Locate every blood parasite and identify its species.
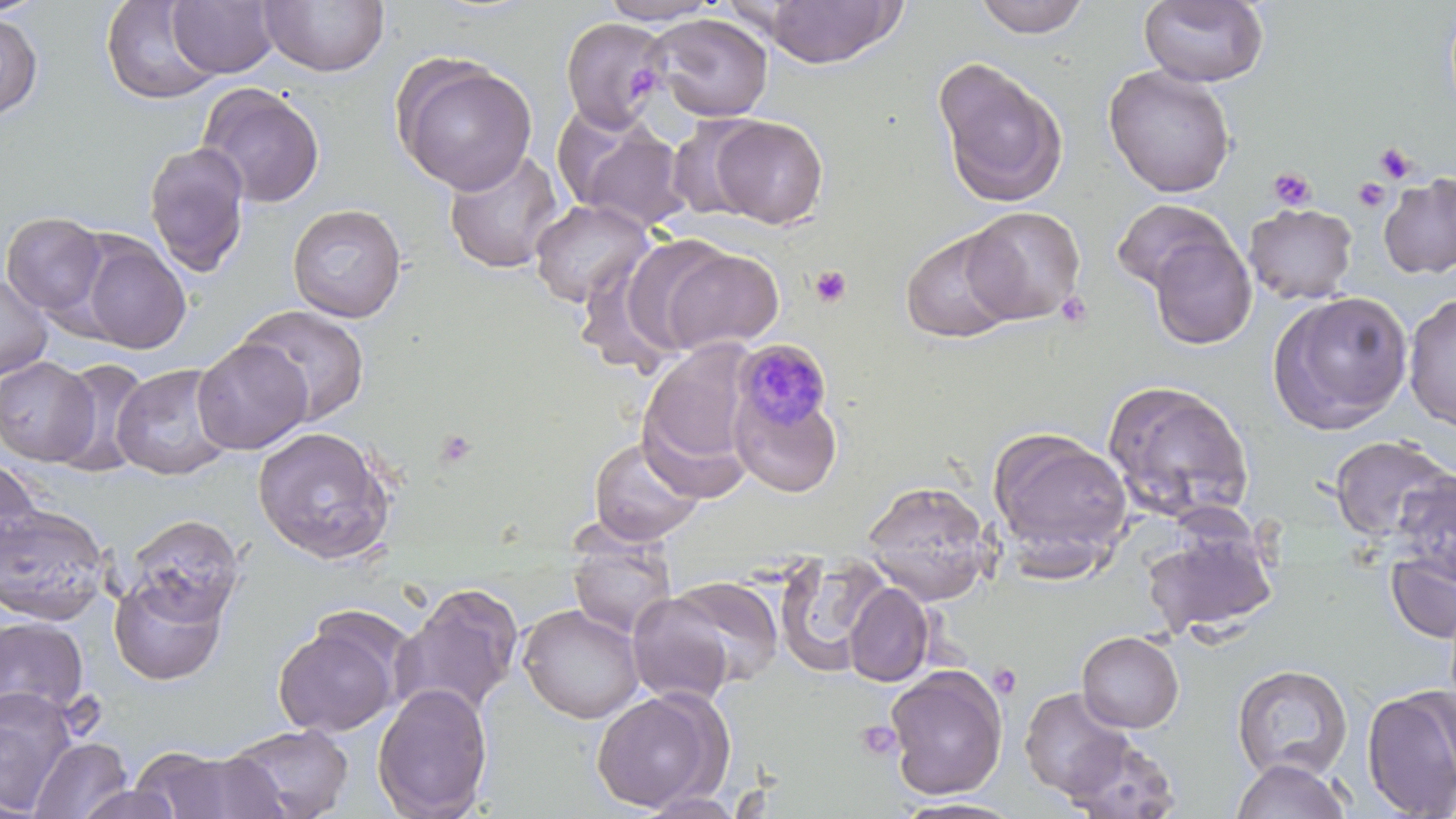

Approximate bounding boxes as [x1, y1, x2, y2] in pixels.
Plasmodium malariae-infected red blood cells: [732, 339, 835, 444].
No Plasmodium falciparum, Plasmodium ovale, Plasmodium vivax, Babesia divergens, or Trypanosoma brucei observed.

Platelet locations: [626, 63, 662, 100], [1375, 143, 1416, 184], [1268, 167, 1317, 211], [1353, 178, 1390, 211], [809, 265, 853, 309], [1054, 290, 1094, 329], [435, 427, 479, 469], [988, 663, 1023, 699], [856, 719, 902, 762]. Uninfected red blood cell locations: [100, 0, 223, 105], [258, 0, 389, 78], [597, 0, 724, 25], [972, 0, 1093, 39], [1139, 0, 1269, 88], [168, 1, 278, 79], [762, 1, 905, 68], [0, 12, 43, 119], [646, 12, 774, 122], [559, 17, 669, 132], [392, 55, 538, 195], [932, 56, 1069, 208], [1102, 64, 1236, 198], [196, 83, 326, 209], [710, 115, 828, 228], [564, 118, 689, 233], [144, 140, 251, 277], [443, 148, 565, 275], [1379, 173, 1456, 279], [529, 199, 654, 308], [1112, 199, 1234, 293], [287, 203, 407, 322], [1243, 203, 1357, 304], [961, 205, 1085, 324], [1, 212, 108, 318], [900, 229, 1021, 343], [1147, 233, 1257, 350], [80, 237, 191, 353], [599, 239, 724, 364], [654, 244, 785, 357], [0, 273, 53, 380], [1267, 289, 1414, 435], [1402, 293, 1456, 431], [237, 304, 371, 426], [193, 338, 312, 453], [639, 339, 756, 482], [0, 356, 98, 466], [50, 358, 152, 476], [110, 363, 236, 480], [1102, 378, 1255, 526], [732, 388, 844, 498], [252, 425, 396, 565], [988, 428, 1134, 569], [1327, 434, 1455, 545], [588, 436, 704, 545], [1, 457, 45, 567], [1392, 471, 1456, 587], [862, 480, 994, 605], [0, 501, 113, 627], [123, 514, 244, 626], [1142, 529, 1277, 639], [567, 535, 677, 640], [1385, 548, 1456, 645], [774, 552, 892, 676], [109, 571, 230, 685], [664, 576, 784, 688], [843, 582, 934, 687], [390, 583, 524, 720], [626, 592, 735, 706], [517, 603, 645, 724], [273, 614, 405, 738], [0, 616, 90, 721], [1076, 630, 1184, 732], [1231, 663, 1354, 782], [886, 665, 1008, 799], [372, 683, 493, 819], [1361, 685, 1456, 819], [1018, 686, 1136, 802], [0, 687, 77, 811], [590, 689, 729, 812], [224, 724, 354, 818], [1062, 735, 1183, 819], [30, 736, 132, 818], [132, 744, 291, 818], [1230, 757, 1352, 819], [73, 784, 185, 819], [635, 791, 747, 818], [891, 796, 1027, 817]. Slide-level diagnosis: Plasmodium malariae. Image is 1456×819 pixels. One field of a larger specimen. Thin blood smear. Light microscopy. Captured at 1000x magnification. May-Grünwald-Giemsa stain.